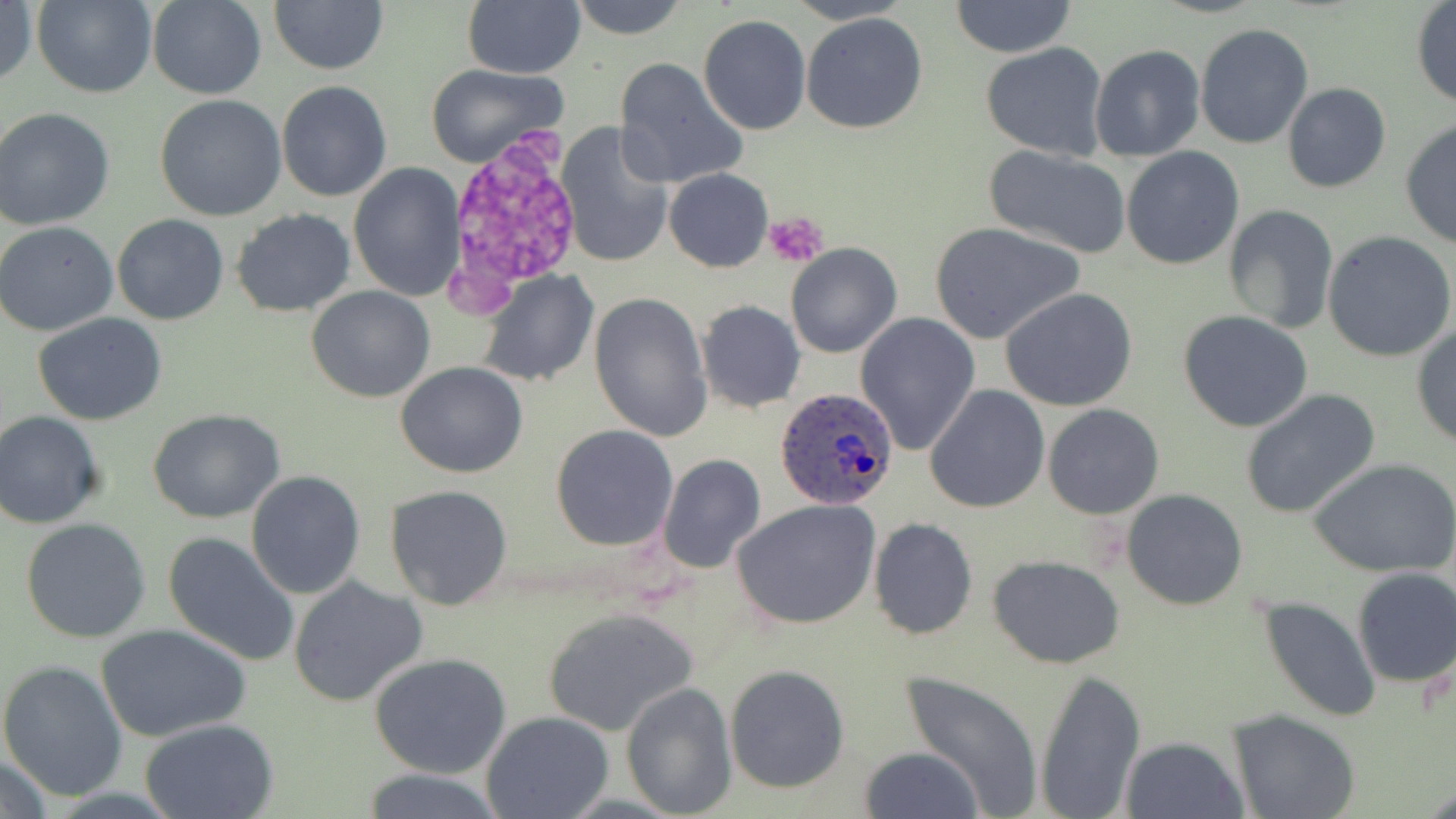

Approximate bounding boxes as named x1/y1/x2/y2 corners in pixels. Platelet locations: (x1=764, y1=210, x2=830, y2=267). Plasmodium ovale-infected red blood cell locations: (x1=775, y1=387, x2=903, y2=512). Uninfected red blood cell locations: (x1=32, y1=0, x2=158, y2=98), (x1=269, y1=0, x2=388, y2=74), (x1=568, y1=0, x2=688, y2=41), (x1=950, y1=0, x2=1076, y2=58), (x1=0, y1=1, x2=37, y2=90), (x1=147, y1=1, x2=267, y2=99), (x1=463, y1=1, x2=585, y2=78), (x1=1410, y1=3, x2=1456, y2=110), (x1=800, y1=12, x2=929, y2=134), (x1=698, y1=13, x2=811, y2=135), (x1=1193, y1=23, x2=1314, y2=149), (x1=980, y1=42, x2=1110, y2=163), (x1=1090, y1=45, x2=1205, y2=162), (x1=613, y1=57, x2=749, y2=189), (x1=425, y1=63, x2=568, y2=168), (x1=276, y1=82, x2=391, y2=202), (x1=1281, y1=82, x2=1391, y2=194), (x1=154, y1=94, x2=288, y2=222), (x1=0, y1=107, x2=115, y2=231), (x1=555, y1=121, x2=674, y2=269), (x1=1399, y1=121, x2=1456, y2=247), (x1=985, y1=144, x2=1130, y2=256), (x1=1122, y1=147, x2=1244, y2=271), (x1=348, y1=164, x2=463, y2=302), (x1=663, y1=168, x2=773, y2=272), (x1=1225, y1=204, x2=1338, y2=334), (x1=232, y1=209, x2=356, y2=317), (x1=112, y1=214, x2=229, y2=326), (x1=0, y1=220, x2=119, y2=335), (x1=929, y1=223, x2=1083, y2=343), (x1=1323, y1=231, x2=1456, y2=362), (x1=785, y1=243, x2=901, y2=360), (x1=477, y1=270, x2=598, y2=387), (x1=307, y1=285, x2=436, y2=402), (x1=999, y1=287, x2=1137, y2=412), (x1=587, y1=290, x2=712, y2=441), (x1=698, y1=300, x2=805, y2=412), (x1=1178, y1=310, x2=1315, y2=432), (x1=855, y1=311, x2=980, y2=453), (x1=32, y1=312, x2=168, y2=424), (x1=1411, y1=323, x2=1456, y2=448), (x1=395, y1=363, x2=528, y2=478), (x1=924, y1=383, x2=1051, y2=515), (x1=1239, y1=388, x2=1382, y2=521), (x1=1043, y1=404, x2=1164, y2=518), (x1=147, y1=408, x2=285, y2=524), (x1=0, y1=411, x2=106, y2=528), (x1=550, y1=424, x2=679, y2=551), (x1=658, y1=454, x2=766, y2=574), (x1=1308, y1=457, x2=1456, y2=577), (x1=246, y1=471, x2=365, y2=598), (x1=386, y1=484, x2=513, y2=611), (x1=1121, y1=489, x2=1250, y2=611), (x1=733, y1=498, x2=882, y2=630), (x1=22, y1=517, x2=150, y2=643), (x1=868, y1=518, x2=978, y2=639), (x1=162, y1=531, x2=300, y2=667), (x1=988, y1=554, x2=1126, y2=668), (x1=1351, y1=568, x2=1456, y2=687), (x1=287, y1=577, x2=427, y2=707), (x1=1259, y1=596, x2=1380, y2=722), (x1=542, y1=606, x2=700, y2=739), (x1=97, y1=624, x2=250, y2=745), (x1=369, y1=652, x2=512, y2=777), (x1=0, y1=660, x2=128, y2=801), (x1=724, y1=664, x2=851, y2=794), (x1=1032, y1=667, x2=1147, y2=819), (x1=899, y1=670, x2=1046, y2=814), (x1=620, y1=682, x2=737, y2=818), (x1=1229, y1=710, x2=1361, y2=819), (x1=481, y1=711, x2=614, y2=819), (x1=141, y1=718, x2=278, y2=818), (x1=1122, y1=737, x2=1248, y2=819), (x1=860, y1=746, x2=984, y2=819), (x1=0, y1=753, x2=58, y2=819), (x1=356, y1=767, x2=510, y2=819). Slide-level diagnosis: Plasmodium ovale. Thin blood film. May-Grünwald-Giemsa-stained preparation. Light microscopy. Image is 1456×819 pixels. One field of a larger specimen. 1000x magnification.